Assess this cell for malaria.
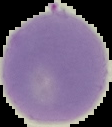
Uninfected.

Summary:
  - Preparation: thin blood smear
  - Image size: 112×127 pixels
  - Image type: segmented cell region on a black background